Name the parasite shown.
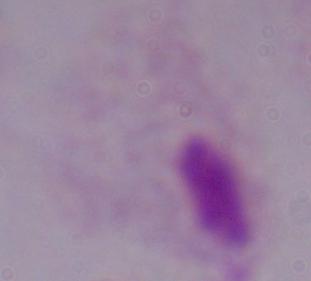

A trichomonad.

Summary:
  - Modality: photomicrograph
  - Magnification: 1000x